State the preparation type.
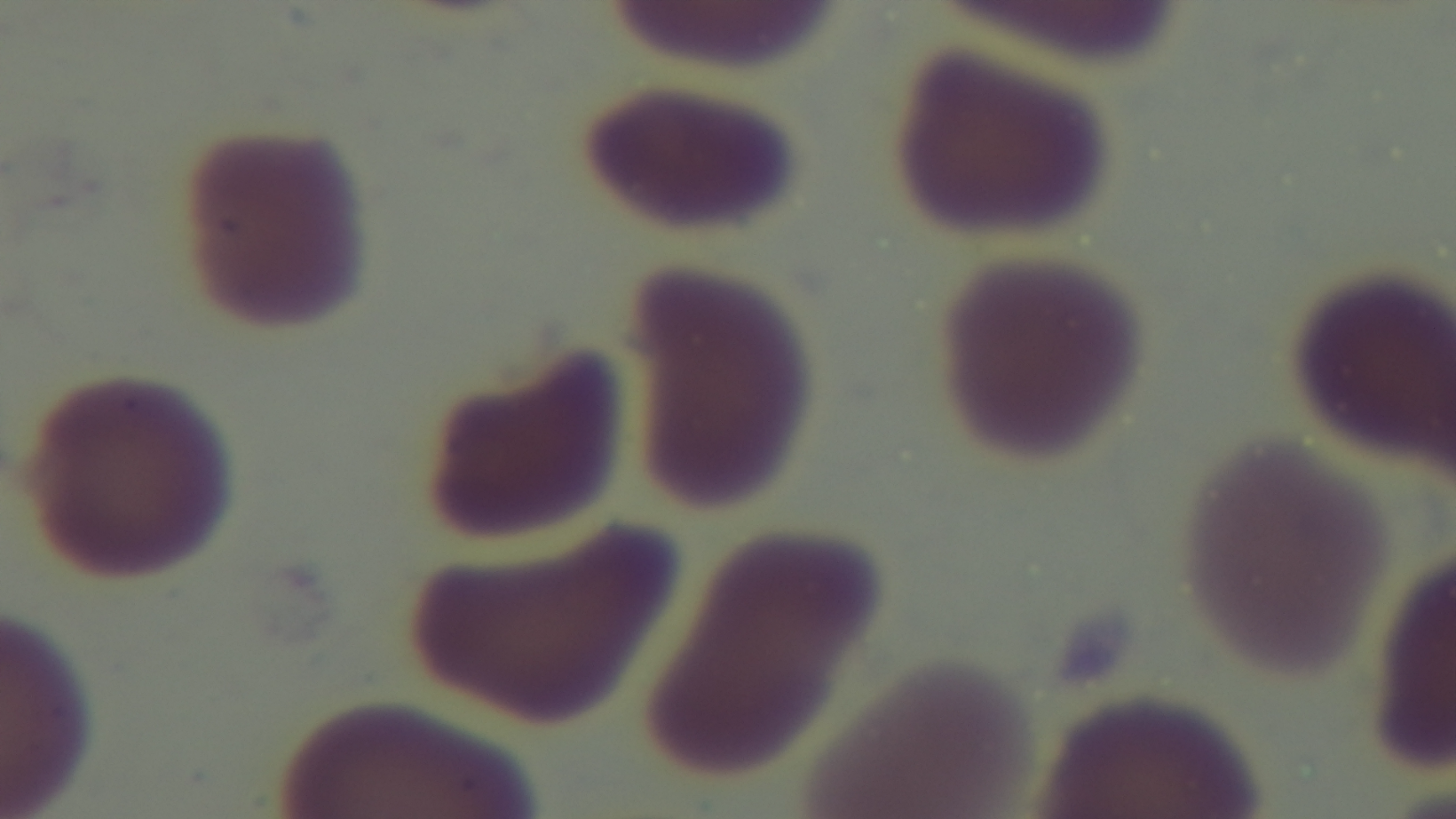

A thin smear.

malaria_status: uninfected
objective: 100x oil immersion
capture: mounted 4K digital camera
modality: light microscopy
stain: Giemsa
field_of_view: single